Assess this cell for malaria.
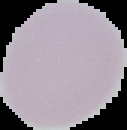

It is uninfected.

preparation = thin blood smear
image type = cell region segmented out of the field of view; surrounding area masked to black
image size = 127×130 pixels